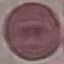
malaria status = uninfected
stain = Giemsa
capture = smartphone camera at the microscope eyepiece
image type = automatically extracted cell patch, resized to 64 × 64 pixels
preparation = thin blood film